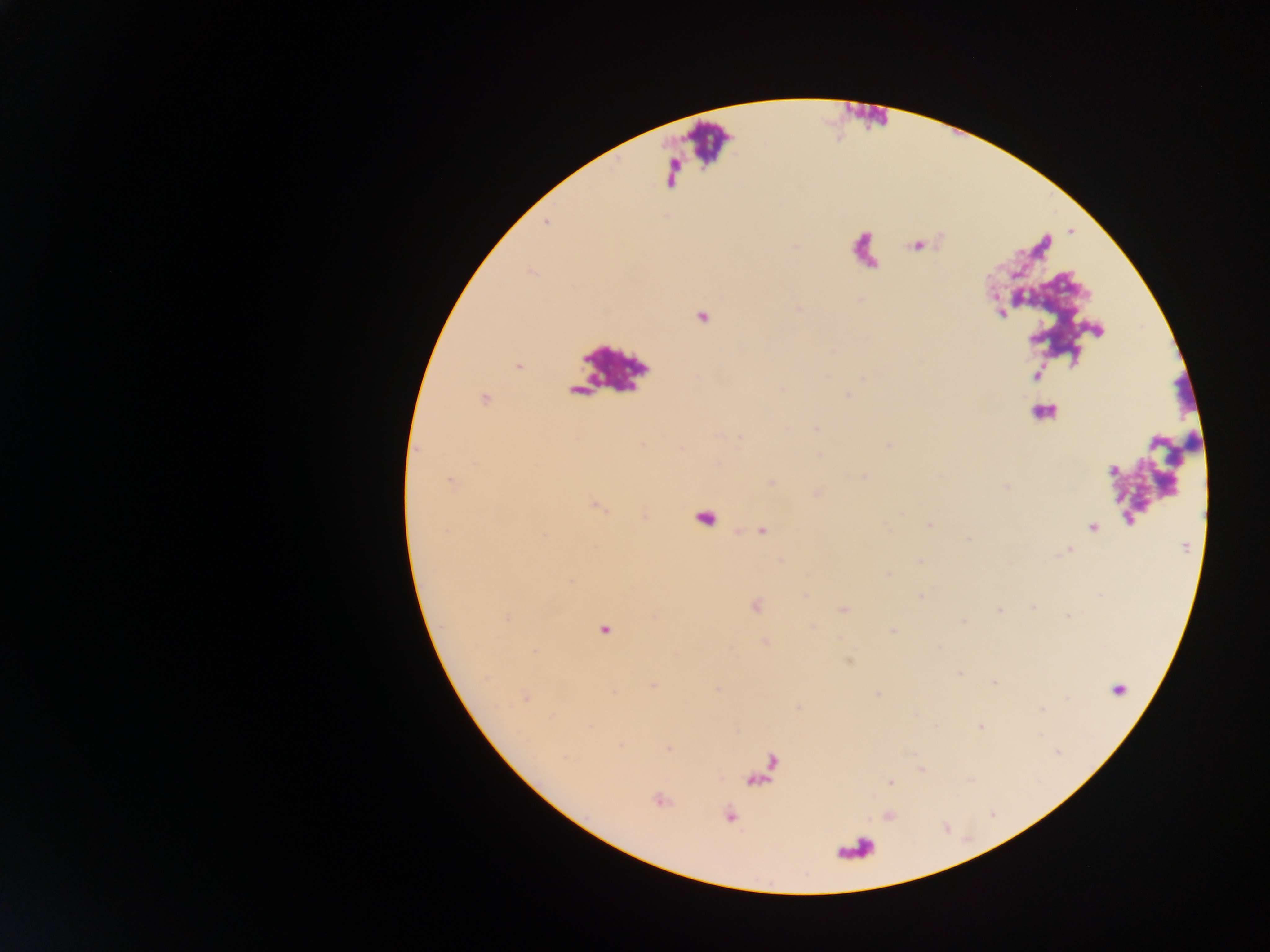

Approximate centers as (x, y) in pixels.
Summary:
  - Malaria parasite locations: (518, 365), (485, 398), (1092, 527), (604, 631), (526, 699), (891, 783), (730, 816)
  - Leukocyte locations: (705, 517)
  - Image size: 1270×952 pixels
  - Country: Ghana
  - Preparation: thick blood film
  - Capture: mobile-phone photograph through a microscope
  - Field of view: single